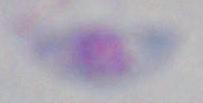
Photomicrograph. Toxoplasma gondii is shown. 1000x magnification.